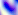

modality: photomicrograph
magnification: 400x
identification: Toxoplasma gondii